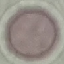
Summary:
  - Malaria status: uninfected
  - Stain: Giemsa
  - Capture: smartphone camera at the microscope eyepiece
  - Image type: cell patch, automatically extracted from a larger field of view and resized to 64 × 64 pixels
  - Preparation: thin blood film